Outline each blood parasite and name the species.
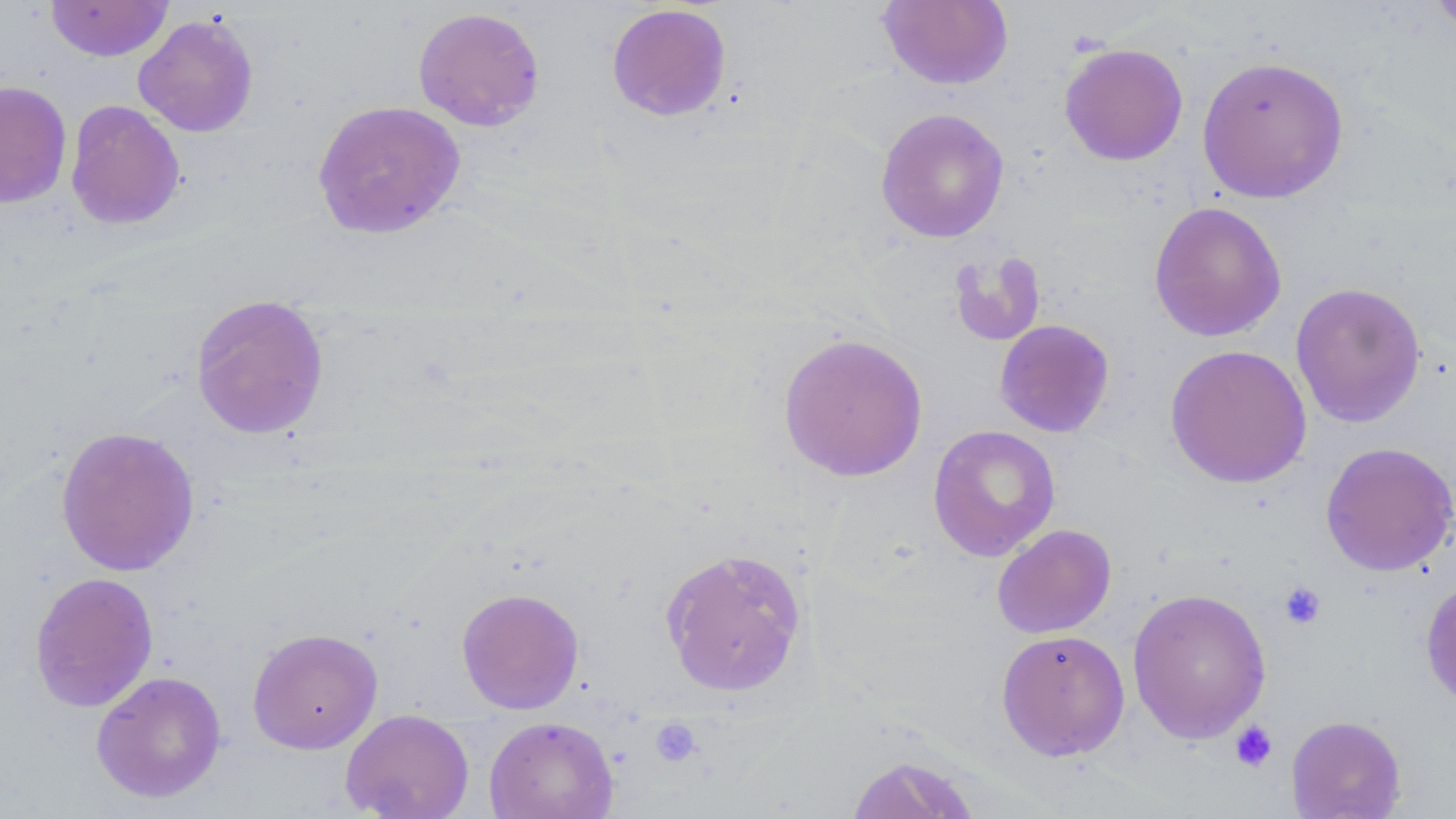
No blood parasites observed.

Summary:
  - Coordinate format: approximate bounding boxes as named x1/y1/x2/y2 corners in pixels
  - Platelet locations: (x1=1278, y1=581, x2=1327, y2=630), (x1=649, y1=716, x2=703, y2=768), (x1=1229, y1=720, x2=1278, y2=773)
  - Uninfected red blood cell locations: (x1=877, y1=0, x2=1014, y2=90), (x1=1426, y1=0, x2=1456, y2=40), (x1=45, y1=1, x2=173, y2=61), (x1=606, y1=3, x2=732, y2=121), (x1=412, y1=6, x2=545, y2=132), (x1=132, y1=14, x2=259, y2=137), (x1=1059, y1=43, x2=1188, y2=166), (x1=1197, y1=55, x2=1350, y2=203), (x1=0, y1=80, x2=73, y2=209), (x1=65, y1=99, x2=185, y2=230), (x1=312, y1=99, x2=466, y2=239), (x1=875, y1=107, x2=1010, y2=243), (x1=1148, y1=200, x2=1287, y2=342), (x1=948, y1=248, x2=1046, y2=347), (x1=1290, y1=281, x2=1427, y2=428), (x1=189, y1=293, x2=329, y2=440), (x1=994, y1=319, x2=1115, y2=438), (x1=777, y1=331, x2=928, y2=482), (x1=1165, y1=343, x2=1312, y2=489), (x1=927, y1=424, x2=1061, y2=561), (x1=55, y1=426, x2=200, y2=577), (x1=1319, y1=441, x2=1456, y2=577), (x1=992, y1=524, x2=1117, y2=638), (x1=659, y1=547, x2=809, y2=698), (x1=29, y1=571, x2=159, y2=713), (x1=1420, y1=576, x2=1456, y2=713), (x1=456, y1=587, x2=585, y2=714), (x1=1127, y1=587, x2=1272, y2=744), (x1=246, y1=627, x2=384, y2=754), (x1=996, y1=628, x2=1130, y2=761), (x1=91, y1=670, x2=227, y2=803), (x1=339, y1=709, x2=475, y2=819), (x1=1286, y1=714, x2=1406, y2=818), (x1=484, y1=715, x2=618, y2=819), (x1=845, y1=754, x2=982, y2=819)
  - Slide-level diagnosis: no evidence of blood parasites
  - Image size: 1456×819 pixels
  - Modality: light microscopy
  - Stain: May-Grünwald-Giemsa
  - Magnification: 1000x
  - Field of view: one of a larger specimen
  - Preparation: thin blood smear